Give the extent of all uninfected red blood cells.
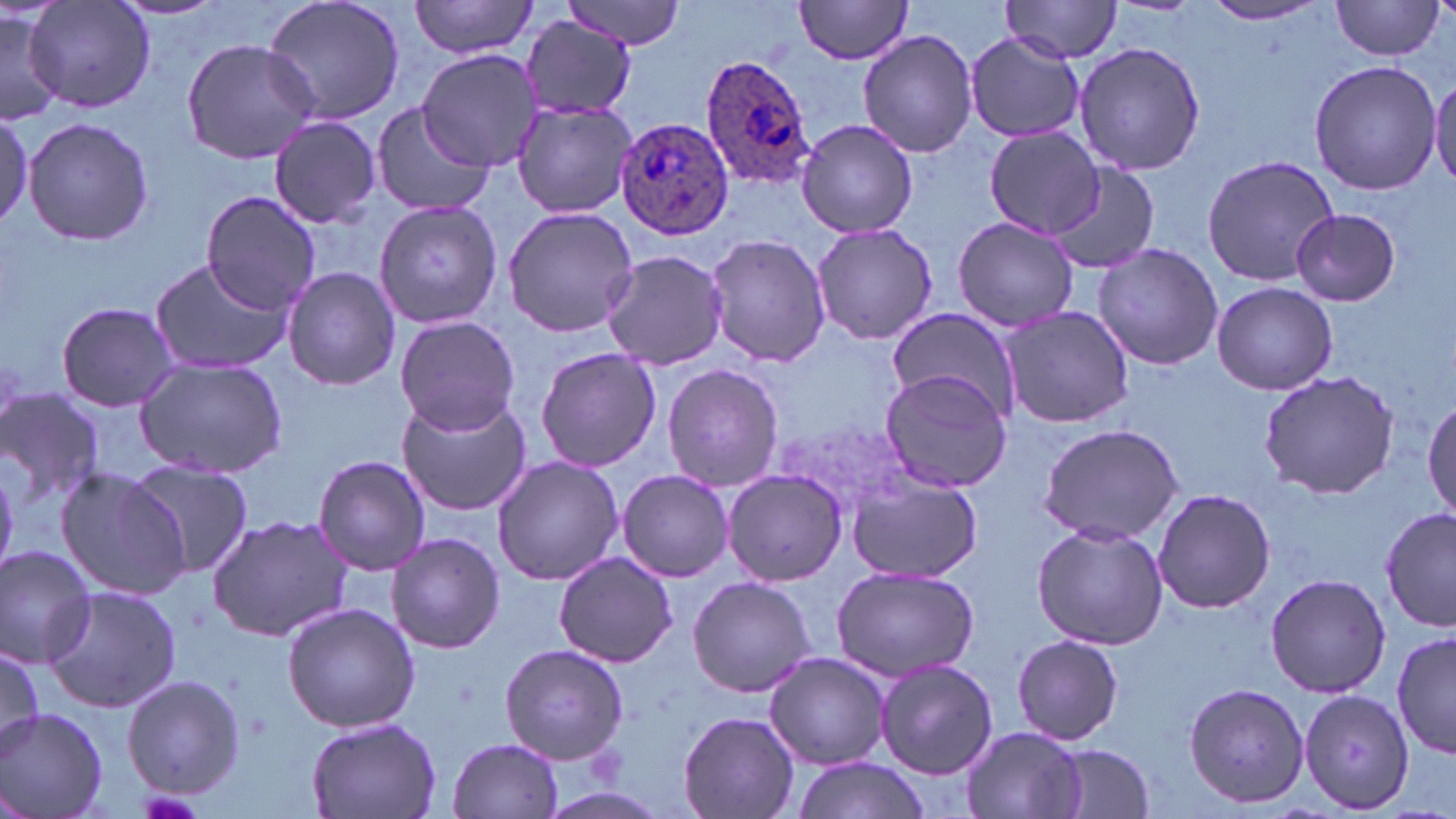
Approximate bounding boxes as [x1, y1, x2, y2] in pixels.
Uninfected red blood cells: [26, 0, 155, 116], [260, 0, 409, 127], [408, 0, 543, 60], [559, 0, 690, 49], [793, 0, 916, 64], [999, 0, 1125, 62], [1331, 1, 1448, 62], [1201, 2, 1331, 25], [0, 9, 65, 124], [521, 16, 637, 120], [858, 28, 980, 158], [963, 32, 1086, 144], [179, 37, 322, 166], [1072, 39, 1207, 178], [419, 51, 544, 171], [1307, 58, 1442, 196], [1429, 74, 1456, 190], [510, 97, 637, 219], [370, 100, 495, 217], [0, 106, 30, 230], [23, 115, 154, 248], [269, 117, 381, 227], [794, 117, 922, 240], [984, 126, 1104, 238], [1199, 154, 1340, 286], [1047, 162, 1159, 277], [201, 191, 323, 313], [374, 200, 504, 328], [502, 205, 639, 338], [1291, 207, 1400, 307], [954, 216, 1078, 332], [810, 222, 938, 346], [702, 233, 830, 367], [1094, 242, 1222, 370], [600, 248, 731, 372], [148, 256, 294, 375], [281, 267, 401, 391], [1209, 282, 1339, 396], [56, 301, 180, 413], [997, 306, 1136, 427], [884, 308, 1017, 421], [395, 315, 518, 434], [535, 347, 662, 471], [134, 356, 288, 479], [661, 361, 783, 493], [878, 369, 1013, 492], [1258, 370, 1401, 500], [0, 389, 103, 513], [395, 393, 534, 517], [1424, 394, 1456, 521], [1036, 424, 1184, 543], [315, 456, 431, 575], [492, 456, 624, 585], [127, 459, 255, 576], [55, 467, 192, 602], [721, 467, 851, 586], [615, 469, 735, 582], [848, 472, 985, 582], [1152, 488, 1276, 614], [1381, 505, 1454, 634], [207, 515, 354, 643], [1030, 520, 1169, 650], [386, 532, 505, 654], [0, 544, 100, 667], [554, 551, 678, 668], [829, 564, 981, 681], [1265, 573, 1391, 697], [687, 576, 817, 699], [41, 585, 184, 715], [283, 602, 420, 733], [1394, 630, 1455, 761], [1011, 634, 1125, 746], [0, 642, 42, 753], [501, 645, 628, 764], [763, 651, 891, 769], [874, 658, 998, 780], [121, 674, 247, 800], [1184, 681, 1312, 808], [1299, 688, 1416, 814], [0, 705, 110, 818], [677, 710, 800, 819], [306, 718, 443, 817], [960, 726, 1091, 819], [450, 737, 565, 818], [1049, 745, 1158, 819], [788, 755, 931, 819].

Plasmodium ovale-infected red blood cell locations: [699, 55, 816, 193], [616, 117, 735, 241]. Slide-level diagnosis: Plasmodium ovale. Single field of view. 1000x magnification. Image is 1456×819 pixels. Thin blood smear. May-Grünwald-Giemsa-stained preparation. Optical microscopy.